Comment on the morphology of the erythrocytes.
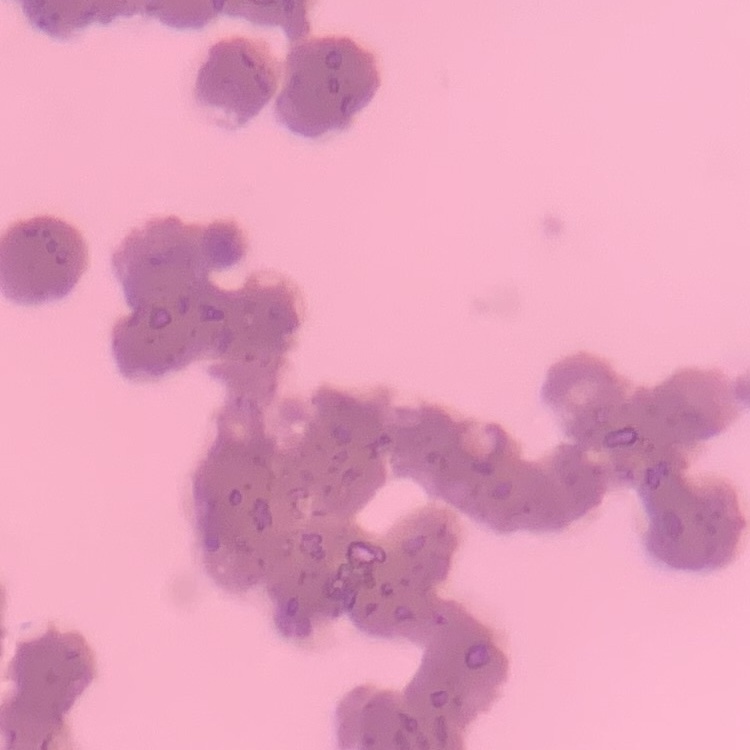

Rouleaux formation.

Summary:
  - Stain: Field's or Giemsa
  - Preparation: thin peripheral smear
  - Image type: square crop of a larger photomicrograph